Assess the morphology of the erythrocytes.
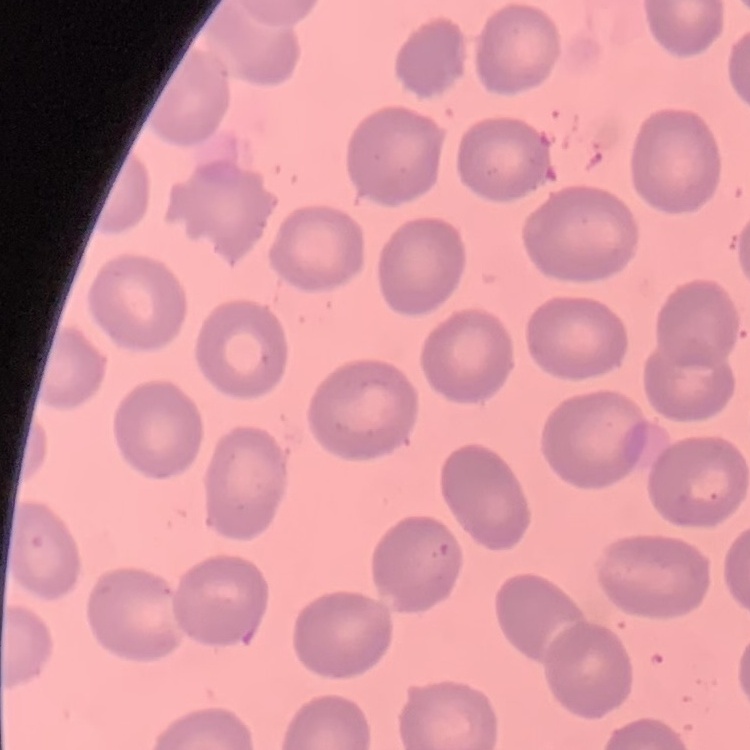
No rouleaux formation.

image type = one tile cut from a larger photomicrograph
preparation = thin blood film
stain = Field's or Giemsa